State the preparation type.
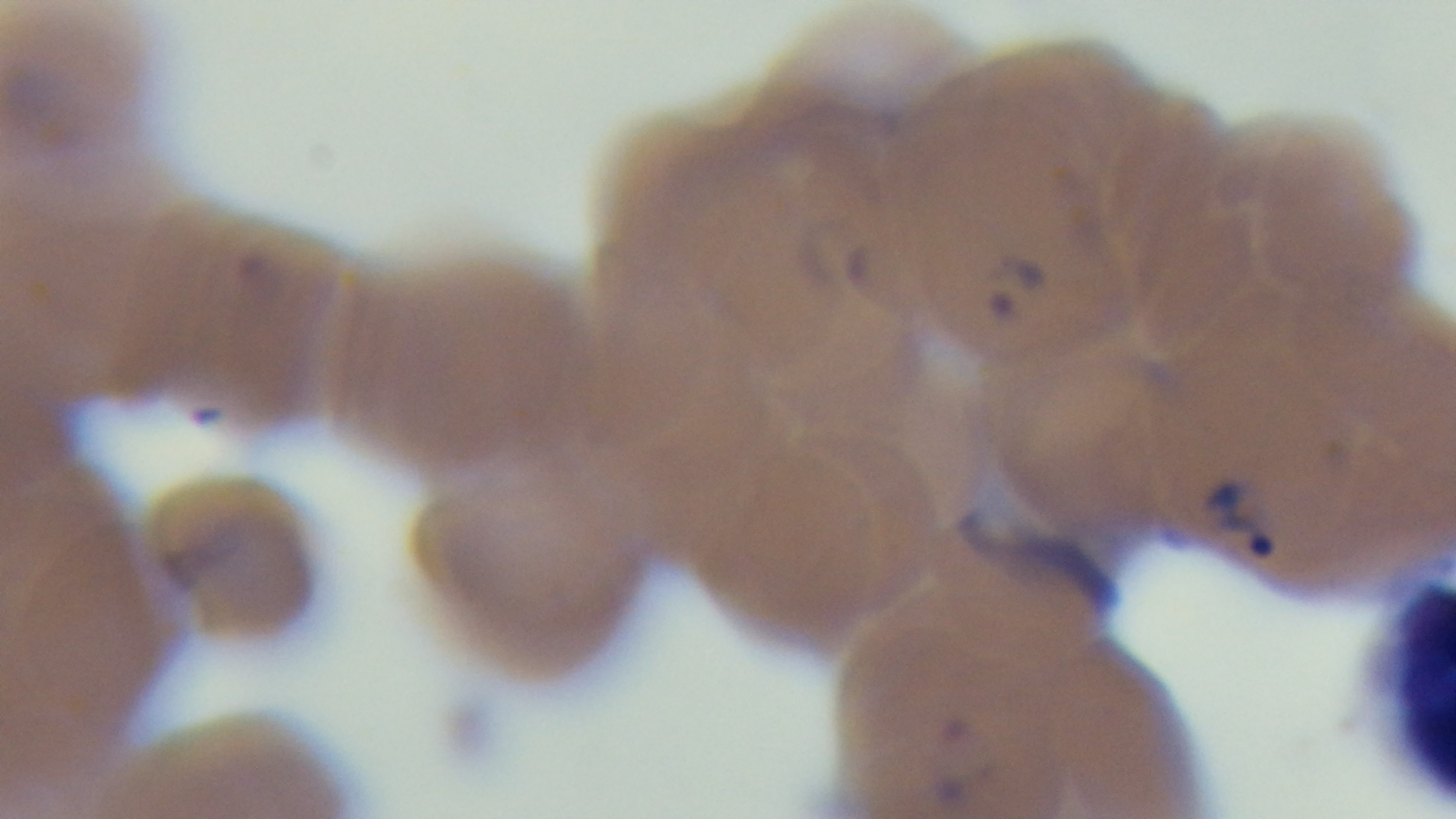

Thin.

Malaria status: infected. Mounted 4K digital camera. One field from the slide. Giemsa stain. Photomicrograph. Oil-immersion objective, 100x.